Locate and identify every blood parasite.
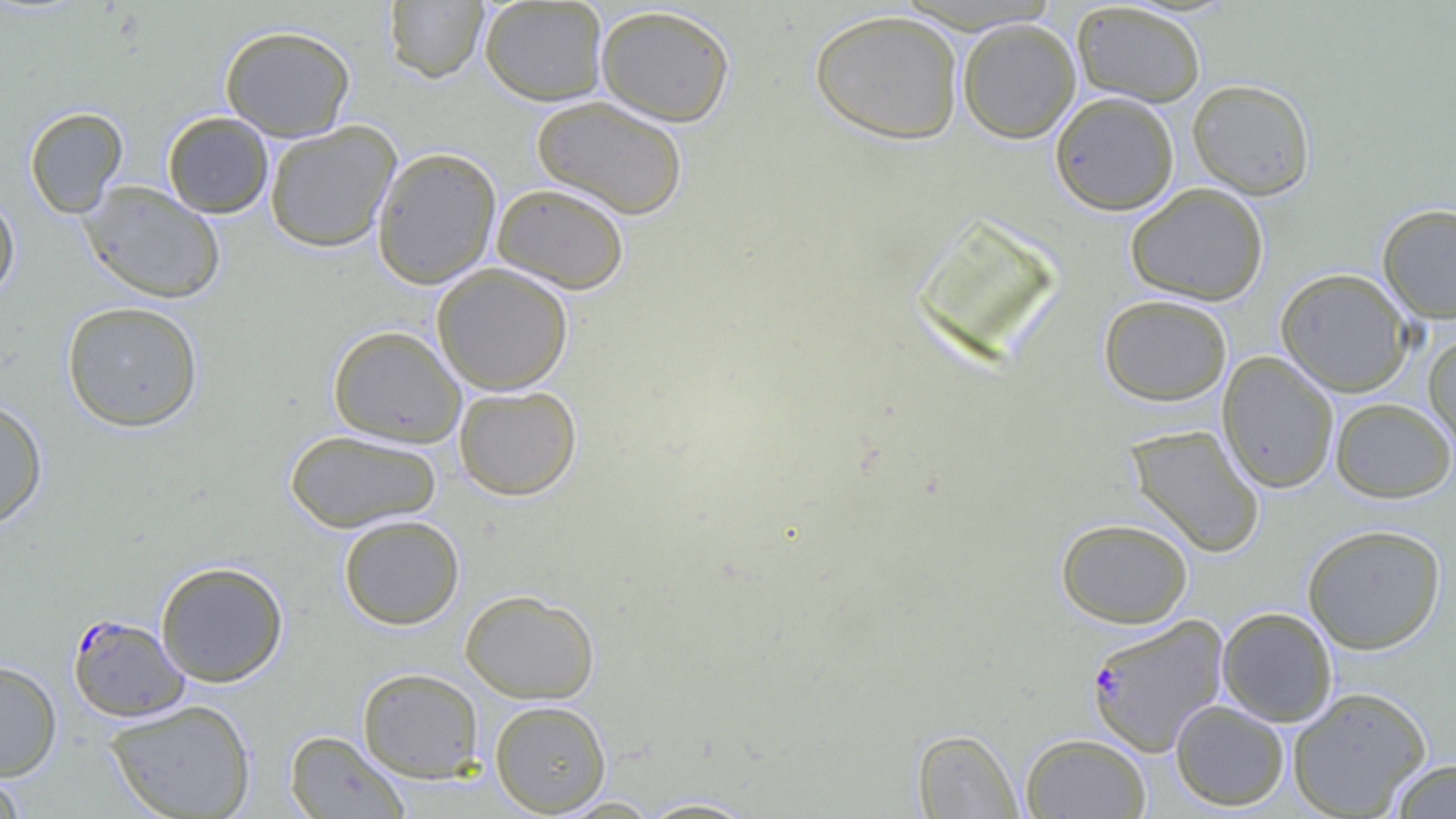
Approximate bounding boxes as (x1, y1, x2, y2) in pixels.
Plasmodium falciparum-infected red blood cells: (67, 613, 190, 723), (1084, 614, 1229, 757).
No Plasmodium ovale, Plasmodium malariae, Plasmodium vivax, Babesia divergens, or Trypanosoma brucei observed.

slide-level diagnosis = Plasmodium falciparum
magnification = 1000x
uninfected red blood cell locations = approximate bounding boxes as (x1, y1, x2, y2) in pixels: (383, 0, 489, 83), (479, 0, 609, 106), (1070, 2, 1207, 108), (594, 4, 736, 126), (809, 8, 965, 144), (957, 17, 1081, 144), (219, 25, 356, 141), (1187, 79, 1316, 199), (1050, 91, 1180, 215), (531, 96, 689, 219), (24, 107, 129, 219), (162, 111, 274, 218), (264, 121, 402, 253), (372, 146, 502, 289), (79, 180, 226, 304), (1125, 182, 1269, 305), (491, 183, 630, 294), (0, 193, 21, 304), (1377, 203, 1456, 323), (431, 263, 574, 395), (1275, 267, 1414, 396), (1098, 293, 1232, 406), (61, 301, 204, 432), (327, 325, 466, 447), (1423, 333, 1456, 457), (1216, 351, 1339, 494), (453, 385, 582, 501), (0, 396, 48, 530), (1329, 397, 1456, 502), (1125, 424, 1265, 557), (283, 429, 442, 532), (338, 515, 465, 630), (1055, 517, 1193, 628), (1302, 523, 1447, 654), (155, 560, 289, 687), (460, 589, 600, 703), (1217, 607, 1338, 727), (0, 660, 62, 781), (356, 667, 485, 783), (1287, 686, 1432, 818), (104, 699, 257, 819), (1170, 699, 1290, 811), (489, 700, 611, 815), (911, 729, 1024, 817), (284, 730, 411, 818), (1020, 733, 1152, 819), (1385, 758, 1456, 818), (0, 770, 27, 818), (633, 797, 762, 818)
image size = 1456×819 pixels
field of view = single
preparation = thin blood smear
modality = light microscopy